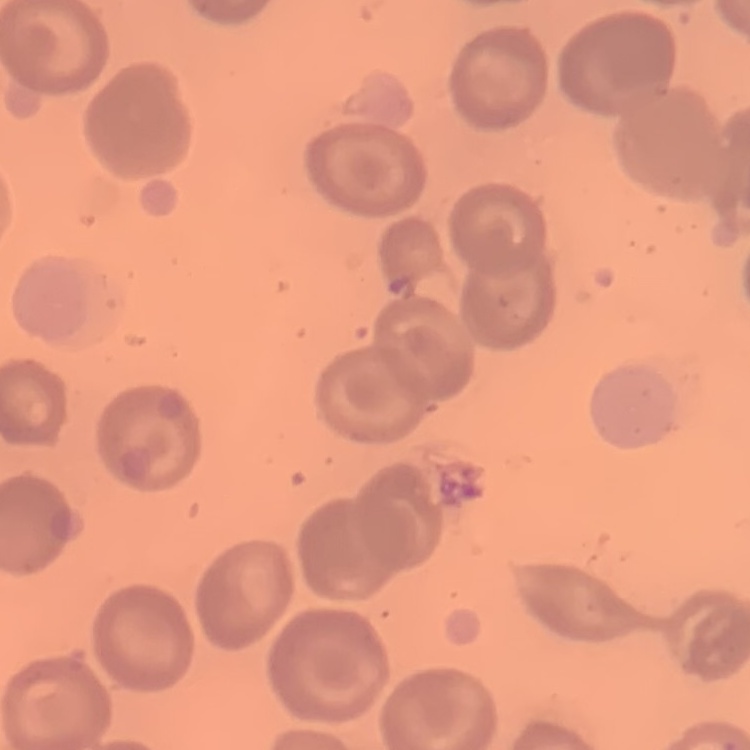

Summary:
  - Erythrocyte morphology: no rouleaux formation
  - Preparation: thin blood film
  - Stain: Field's or Giemsa
  - Image type: square crop of a larger photomicrograph